Locate and identify every blood parasite.
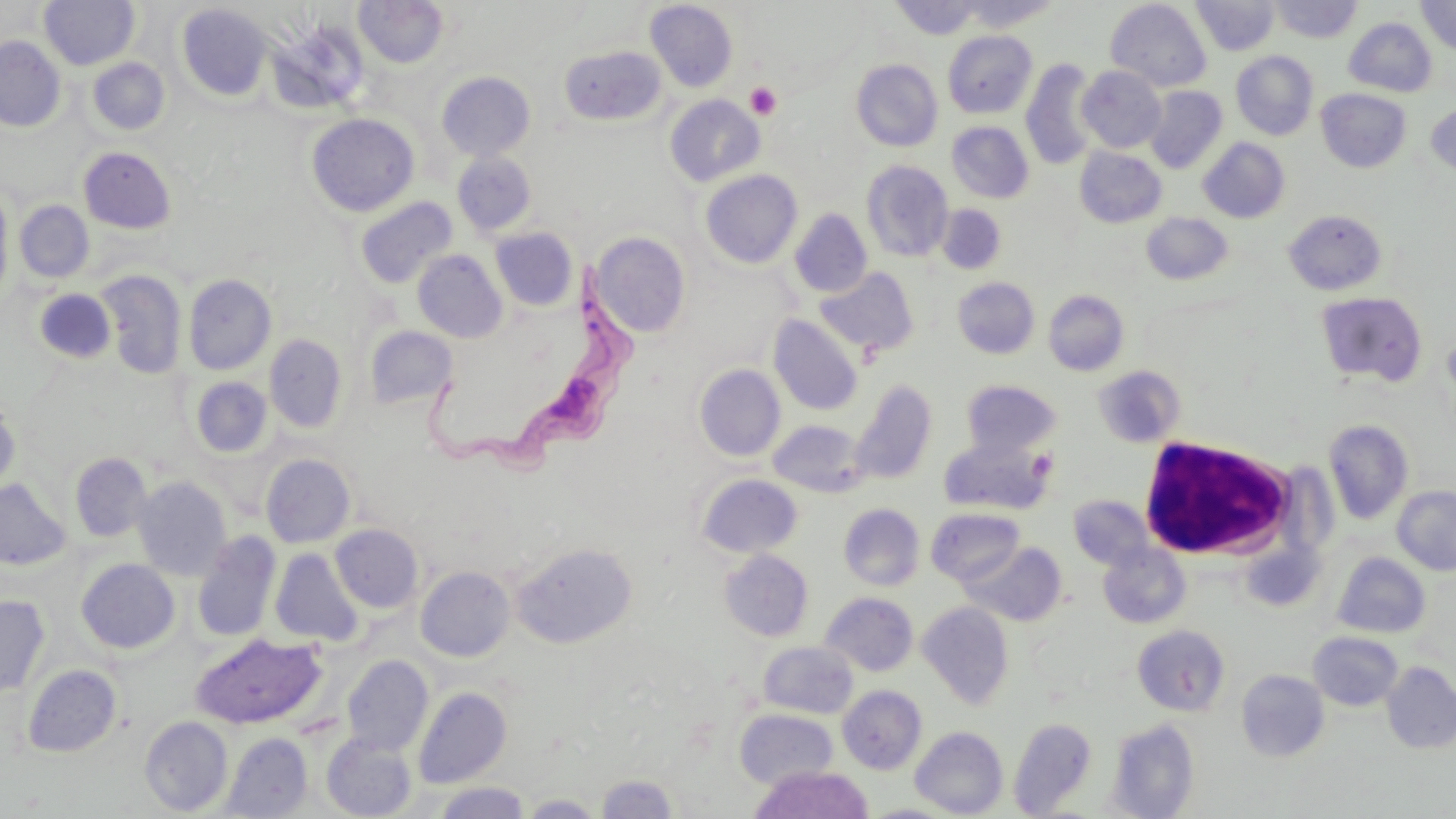

Approximate bounding boxes as (x1, y1, x2, y2) in pixels.
Trypanosoma brucei: (416, 259, 637, 490).
No Plasmodium falciparum, Plasmodium ovale, Plasmodium malariae, Plasmodium vivax, or Babesia divergens observed.

slide-level diagnosis = Trypanosoma brucei
field of view = single
stain = May-Grünwald-Giemsa
preparation = thin blood smear
uninfected red blood cell locations = approximate bounding boxes as (x1, y1, x2, y2) in pixels: (39, 0, 139, 69), (353, 0, 450, 68), (890, 0, 984, 40), (954, 0, 1060, 31), (1192, 0, 1280, 55), (1269, 0, 1362, 43), (1416, 0, 1456, 55), (645, 1, 738, 92), (1105, 1, 1212, 92), (177, 4, 273, 101), (1344, 17, 1437, 97), (277, 25, 369, 113), (943, 30, 1038, 119), (0, 36, 65, 131), (559, 46, 666, 125), (1230, 51, 1318, 140), (88, 58, 169, 135), (851, 59, 943, 151), (1021, 59, 1100, 170), (1077, 66, 1166, 152), (437, 71, 535, 161), (1144, 86, 1227, 174), (1316, 89, 1411, 173), (665, 94, 765, 187), (1427, 103, 1456, 177), (306, 113, 419, 217), (947, 121, 1034, 203), (1198, 137, 1290, 223), (79, 146, 176, 233), (1075, 147, 1167, 228), (452, 152, 537, 236), (861, 160, 954, 262), (700, 169, 803, 269), (0, 185, 14, 303), (354, 197, 458, 288), (15, 200, 94, 282), (937, 205, 1006, 275), (789, 209, 873, 297), (1284, 209, 1387, 295), (1141, 212, 1232, 285), (491, 227, 578, 311), (592, 232, 690, 337), (412, 249, 507, 342), (814, 266, 919, 357), (95, 269, 188, 379), (183, 274, 276, 375), (953, 277, 1040, 359), (33, 288, 117, 365), (1043, 289, 1129, 376), (1315, 291, 1428, 388), (769, 315, 863, 415), (364, 326, 458, 410), (264, 334, 347, 432), (694, 364, 785, 461), (1094, 366, 1184, 447), (191, 376, 272, 458), (849, 380, 937, 485), (961, 380, 1061, 457), (0, 395, 20, 494), (768, 420, 869, 497), (1323, 420, 1414, 524), (940, 436, 1053, 515), (70, 453, 152, 542), (260, 453, 356, 548), (697, 474, 803, 558), (132, 476, 231, 580), (0, 479, 70, 570), (1392, 485, 1456, 574), (1068, 495, 1153, 569), (838, 503, 925, 591), (926, 507, 1025, 586), (330, 524, 423, 613), (192, 532, 281, 642), (511, 541, 637, 648), (962, 542, 1066, 627), (1242, 542, 1322, 611), (1098, 544, 1190, 628), (270, 548, 363, 646), (720, 549, 813, 641), (1332, 551, 1431, 638), (76, 559, 180, 653), (416, 566, 515, 662), (821, 592, 918, 676), (0, 595, 49, 696), (917, 602, 1014, 710), (1132, 625, 1230, 715), (1308, 631, 1404, 711), (191, 633, 325, 729), (758, 641, 858, 718), (342, 655, 433, 756), (1381, 662, 1456, 754), (23, 664, 122, 757), (1237, 669, 1330, 761), (838, 685, 927, 774), (414, 686, 512, 788), (735, 709, 838, 789), (140, 715, 233, 815), (1008, 717, 1098, 816), (1107, 719, 1200, 818), (910, 726, 1008, 817), (222, 732, 313, 818), (321, 734, 417, 819), (749, 765, 874, 819), (596, 774, 680, 818), (433, 782, 530, 819), (521, 794, 605, 817), (861, 803, 957, 818)
white blood cell locations = approximate bounding boxes as (x1, y1, x2, y2) in pixels: (1138, 435, 1299, 562)
modality = light microscopy
image size = 1456×819 pixels
platelet locations = approximate bounding boxes as (x1, y1, x2, y2) in pixels: (745, 82, 782, 119)
magnification = 1000x